Report the malaria status.
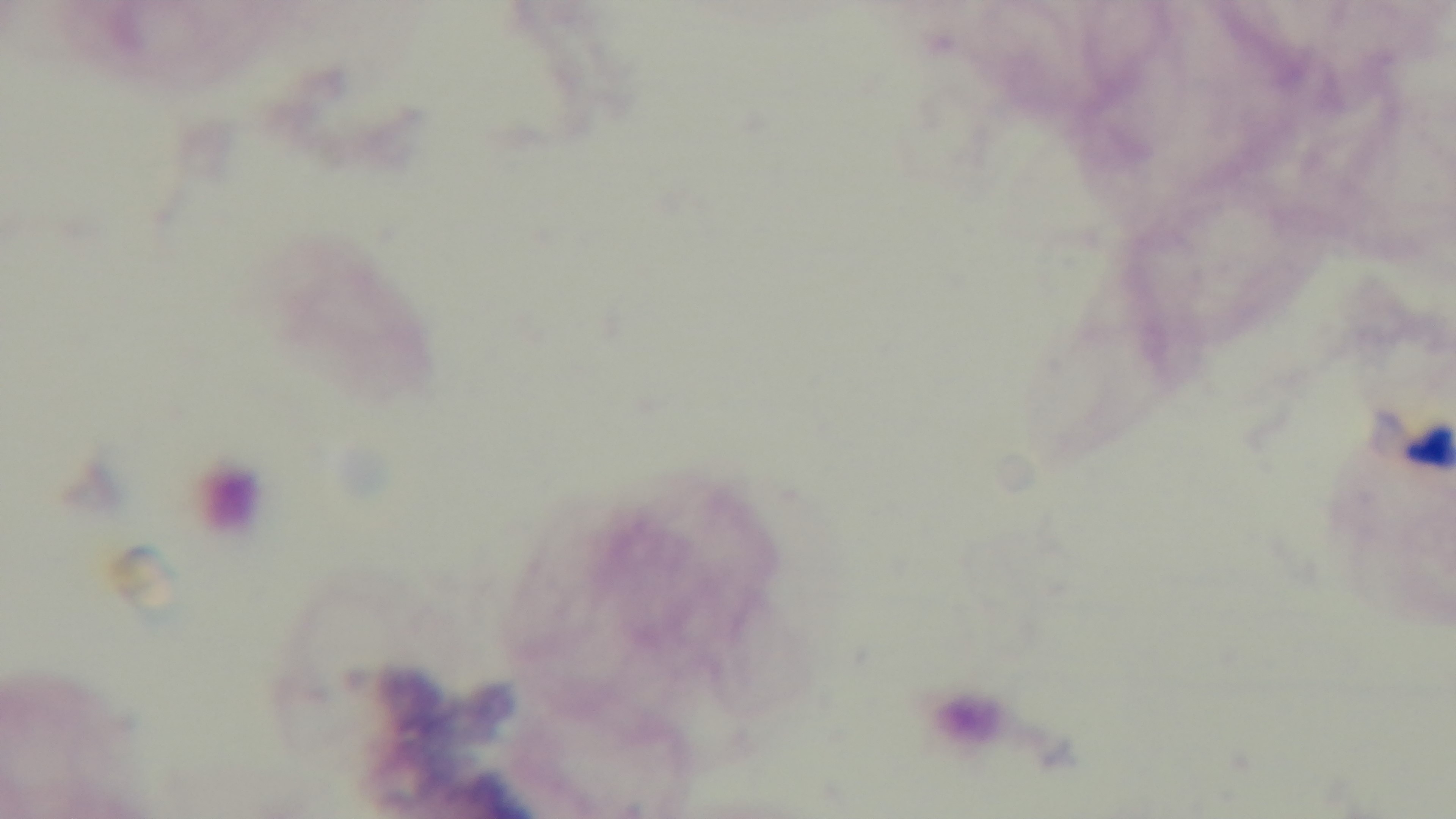

It is uninfected.

Summary:
  - Capture: mounted 4K digital camera
  - Field of view: one from the slide
  - Stain: Giemsa
  - Modality: light microscopy
  - Objective: 100x oil immersion
  - Preparation: thick